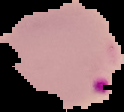
image_size: 124×112 pixels
preparation: thin blood smear
malaria_status: parasitized
image_type: segmented cell region on a black background